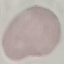
Summary:
  - Malaria status: uninfected
  - Capture: smartphone camera at the microscope eyepiece
  - Preparation: thin blood film
  - Image type: cell patch, automatically extracted from a larger field of view and resized to 64 × 64 pixels
  - Stain: Giemsa